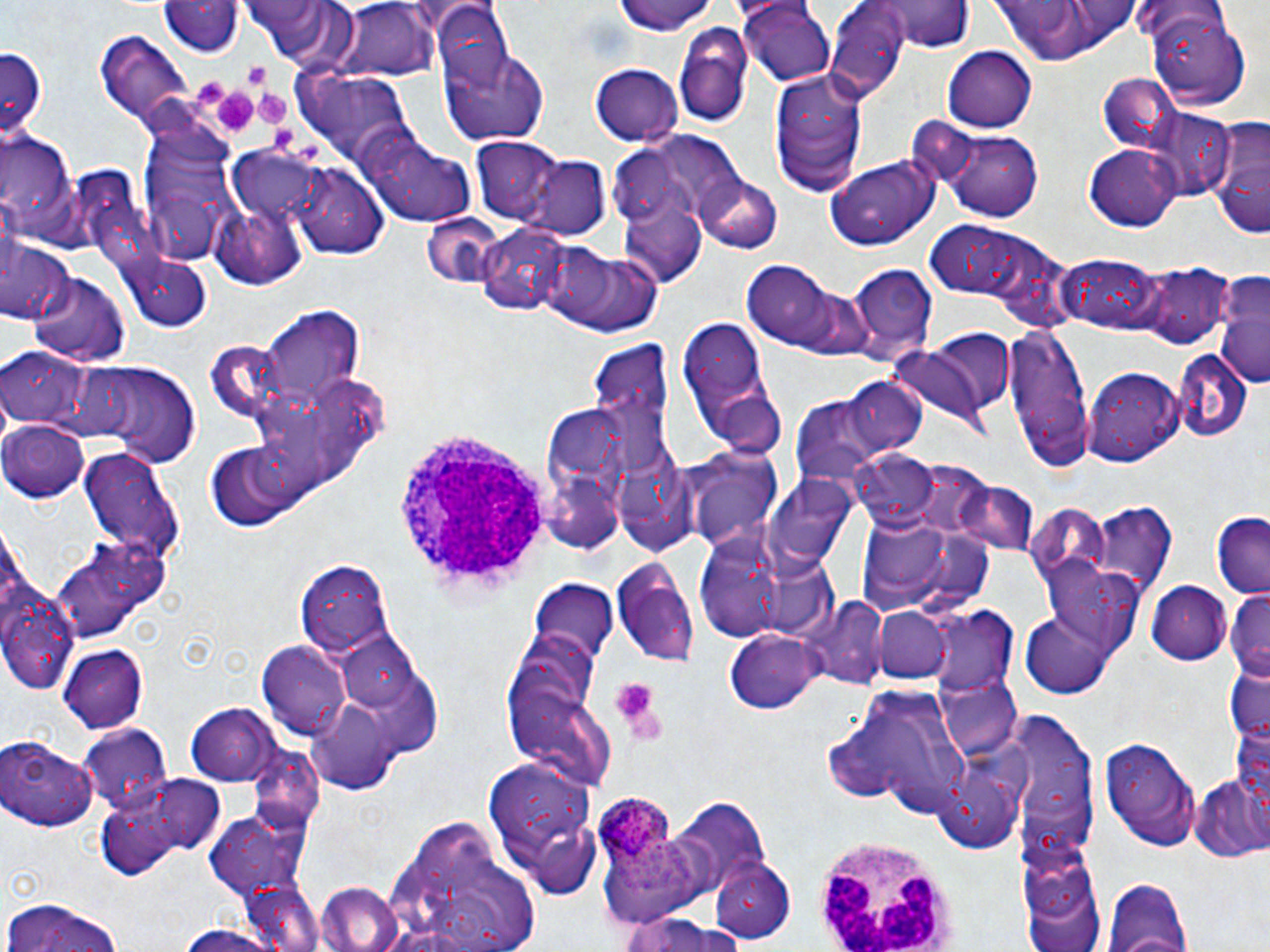

slide-level diagnosis = Plasmodium ovale
image size = 1270×952 pixels
field of view = single
stain = May-Grünwald-Giemsa
magnification = 1000x
preparation = thin blood film
uninfected red blood cell locations = approximate bounding boxes as (x1, y1, x2, y2) in pixels: (610, 0, 720, 37), (159, 1, 242, 58), (239, 1, 362, 70), (338, 1, 439, 82), (871, 1, 973, 54), (986, 2, 1132, 66), (739, 3, 836, 86), (430, 5, 509, 87), (825, 6, 908, 100), (1149, 9, 1252, 109), (673, 23, 754, 128), (95, 31, 194, 133), (0, 45, 49, 141), (440, 45, 551, 146), (942, 45, 1038, 132), (590, 64, 683, 146), (768, 67, 868, 193), (298, 69, 413, 167), (1099, 74, 1178, 152), (1141, 107, 1233, 199), (1205, 115, 1270, 242), (137, 122, 240, 261), (944, 128, 1040, 220), (0, 132, 79, 238), (369, 134, 474, 226), (471, 137, 562, 224), (1084, 145, 1181, 230), (524, 155, 611, 240), (825, 156, 939, 250), (290, 163, 387, 258), (694, 173, 783, 254), (617, 184, 709, 289), (210, 196, 309, 290), (419, 213, 510, 290), (477, 220, 579, 317), (926, 222, 1073, 319), (2, 237, 75, 327), (540, 246, 665, 339), (1059, 254, 1169, 335), (118, 255, 211, 334), (743, 257, 861, 351), (850, 265, 937, 360), (1134, 265, 1231, 350), (29, 272, 130, 366), (1213, 274, 1270, 390), (261, 306, 363, 411), (678, 317, 782, 459), (1006, 327, 1094, 472), (888, 344, 995, 433), (1174, 347, 1252, 441), (1, 349, 82, 425), (73, 357, 201, 468), (1084, 366, 1186, 465), (845, 377, 924, 458), (789, 394, 890, 487), (2, 421, 89, 503), (202, 441, 309, 532), (75, 444, 184, 564), (684, 447, 785, 552), (853, 450, 937, 529), (767, 474, 861, 571), (951, 480, 1040, 558), (1091, 502, 1177, 599), (852, 511, 994, 621), (1209, 513, 1269, 597), (693, 534, 783, 640), (50, 541, 158, 645), (611, 556, 699, 673), (296, 559, 394, 661), (1032, 562, 1144, 673), (527, 579, 620, 661), (1147, 580, 1231, 667), (1225, 591, 1270, 682), (804, 596, 887, 689), (4, 603, 73, 692), (927, 607, 1018, 696), (871, 608, 952, 684), (1022, 610, 1118, 696), (724, 629, 820, 714), (332, 630, 426, 716), (258, 640, 353, 739), (500, 642, 605, 775), (58, 644, 147, 733), (1225, 666, 1270, 746), (936, 668, 1020, 762), (845, 689, 979, 815), (303, 696, 405, 793), (186, 703, 279, 786), (1007, 713, 1097, 849), (1230, 717, 1270, 815), (78, 726, 173, 814), (1100, 732, 1200, 848), (1, 733, 100, 832), (932, 756, 1024, 855), (483, 760, 599, 900), (102, 773, 229, 874), (1190, 774, 1270, 864), (669, 795, 769, 894), (204, 804, 313, 902), (383, 821, 544, 952), (709, 857, 797, 944), (1100, 873, 1196, 952), (1023, 874, 1107, 952), (313, 881, 404, 952), (2, 898, 129, 952), (617, 914, 739, 952), (170, 924, 289, 952)
Plasmodium ovale-infected red blood cell locations = approximate bounding boxes as (x1, y1, x2, y2) in pixels: (596, 800, 694, 895)
modality = light microscopy
platelet locations = approximate bounding boxes as (x1, y1, x2, y2) in pixels: (243, 62, 269, 87), (206, 85, 259, 139), (258, 92, 289, 124), (272, 127, 296, 151), (608, 677, 662, 735)
white blood cell locations = approximate bounding boxes as (x1, y1, x2, y2) in pixels: (391, 419, 558, 601), (815, 835, 957, 951)